Comment on the morphology of the erythrocytes.
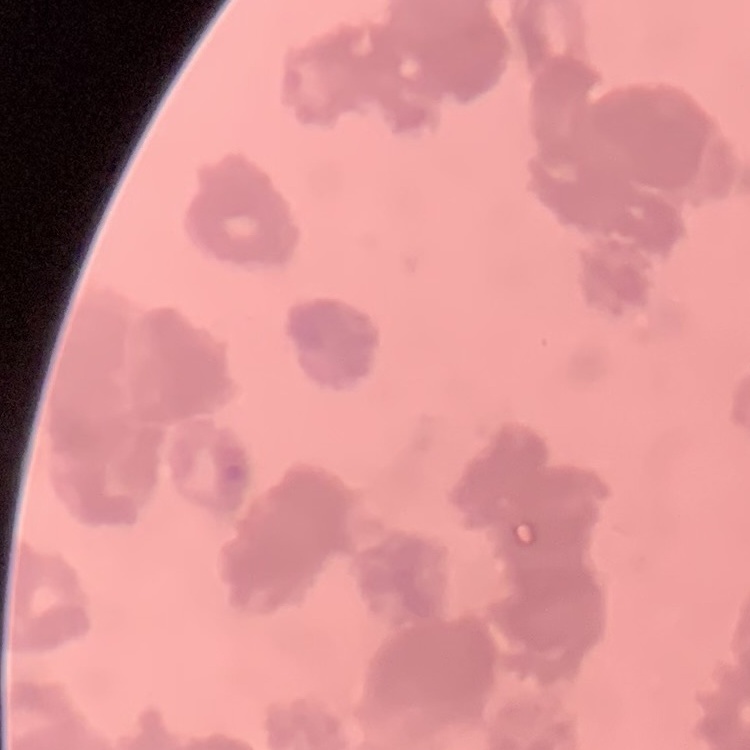
Rouleaux formation.

Thin peripheral smear. Square crop of a larger photomicrograph. Stained with either Field's or Giemsa.